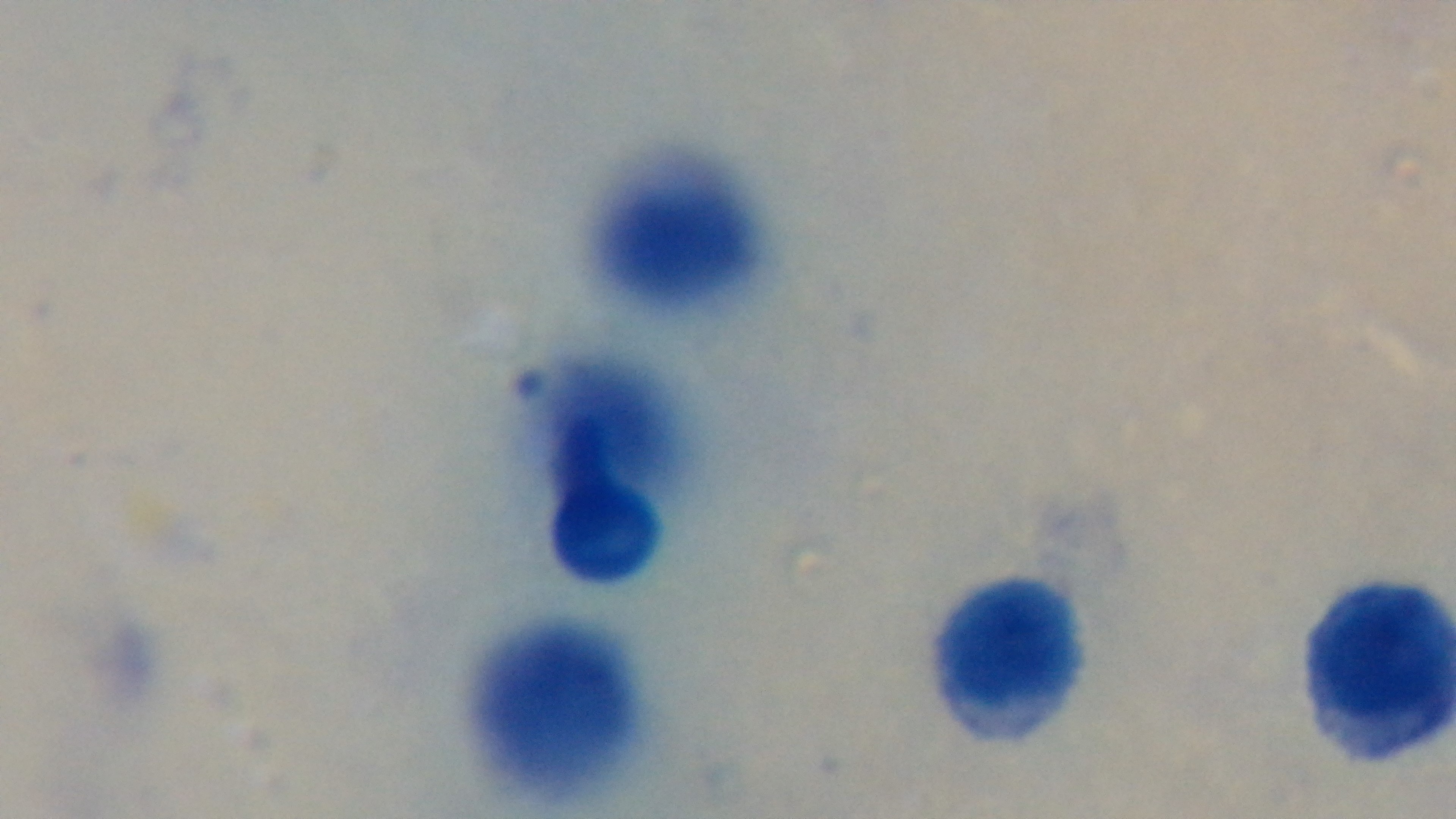

Summary:
  - Preparation: thick
  - Stain: Giemsa
  - Capture: mounted 4K digital camera
  - Malaria status: uninfected
  - Field of view: one from the slide
  - Objective: 100x oil immersion
  - Modality: light microscopy